Locate every leukocyte (white blood cell).
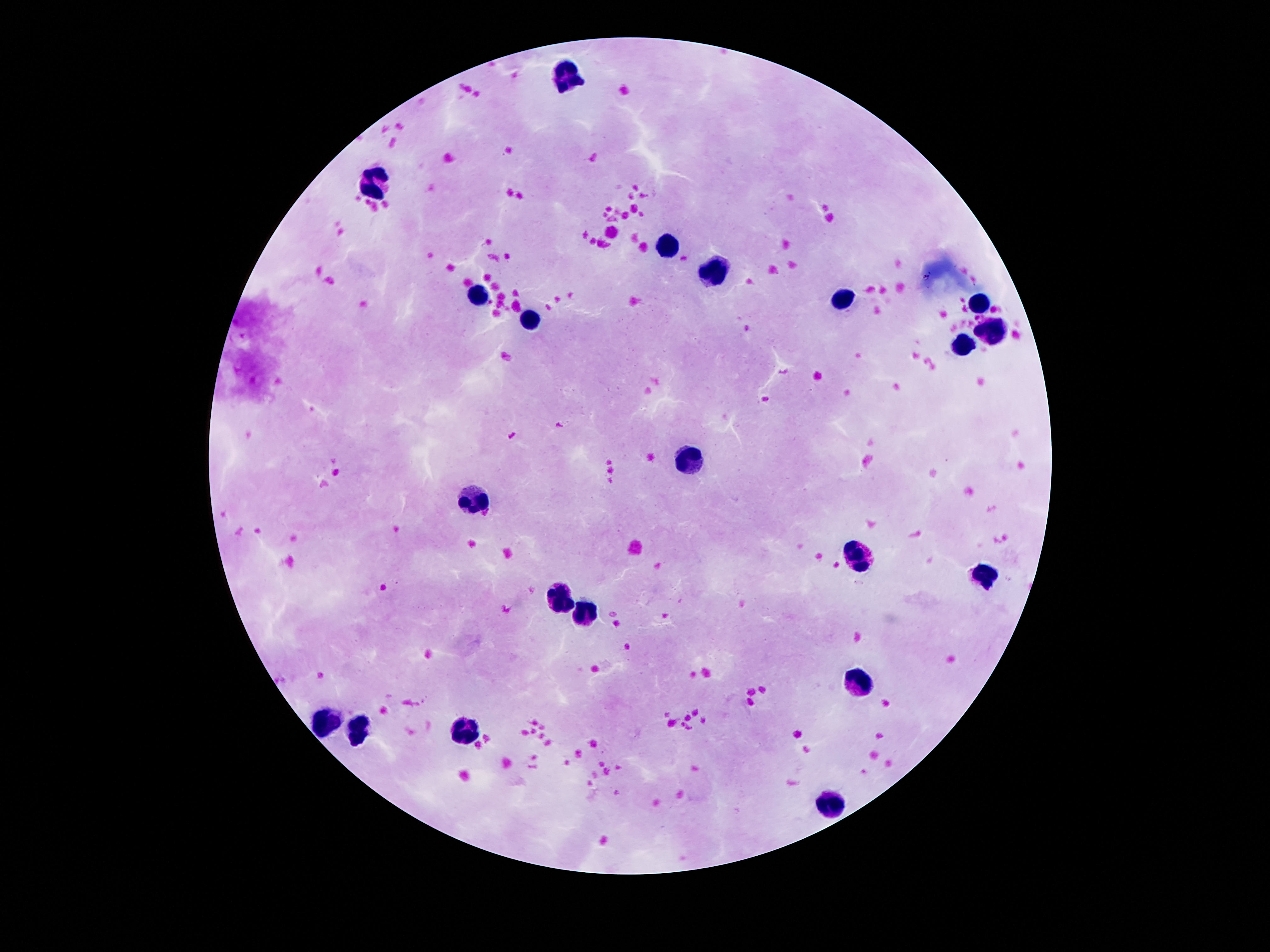

Approximate centers as (x, y) in pixels.
Leukocytes: (566, 72), (379, 180), (670, 247), (715, 269), (477, 293), (843, 299), (979, 303), (530, 320), (992, 330), (964, 345), (685, 458), (475, 497), (859, 559), (983, 577), (563, 598), (586, 613), (862, 682), (323, 722), (362, 729), (465, 731), (832, 800).

{
  "patient_malaria_status": "not infected",
  "image_size": "1270×952 pixels",
  "magnification": "100x",
  "stain": "Giemsa",
  "field_of_view": "one from this slide",
  "preparation": "thick blood film",
  "capture": "smartphone camera through the microscope eyepiece"
}